Assess the morphology of the erythrocytes.
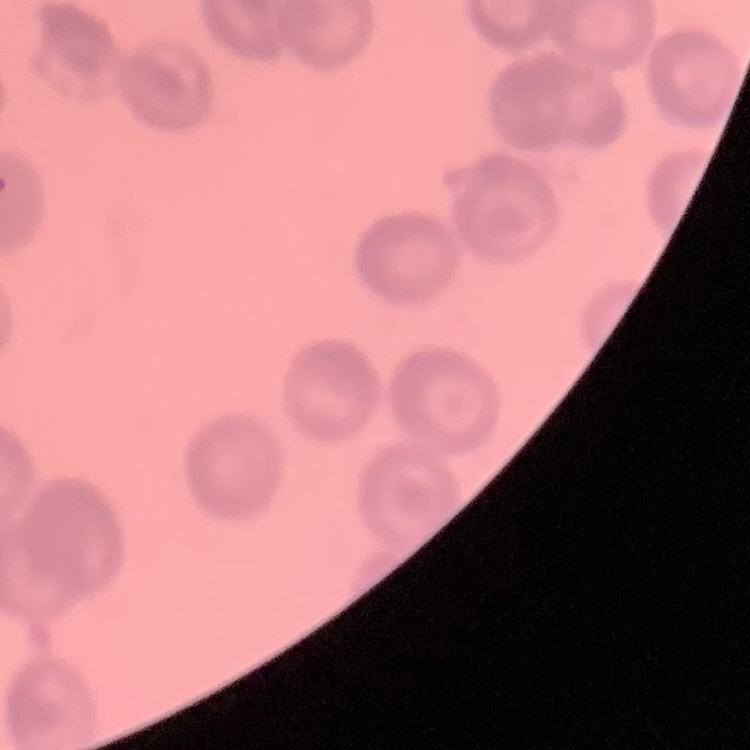

They show rouleaux formation.

Thin blood smear. Stained with either Field's or Giemsa. One tile cut from a larger photomicrograph.